Give the position of every malaria parasite.
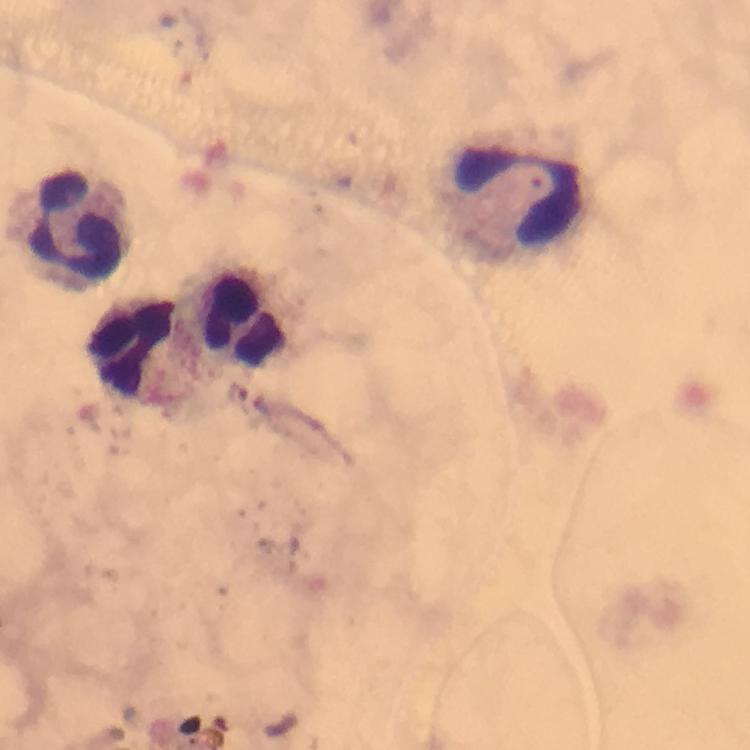

No malaria parasites seen.

{
  "stain": "Giemsa",
  "capture": "smartphone camera through the microscope",
  "cropped_from": "one field of view",
  "image_size": "750×750 pixels",
  "magnification": "100x",
  "leukocyte_locations": "approximate centers as (x, y) in pixels: (524, 198), (82, 226), (243, 315), (137, 345)",
  "context": "from a diagnostic examination for malaria",
  "immersion_oil": "applied",
  "preparation": "thick blood smear"
}